Locate leukocytes (white blood cells).
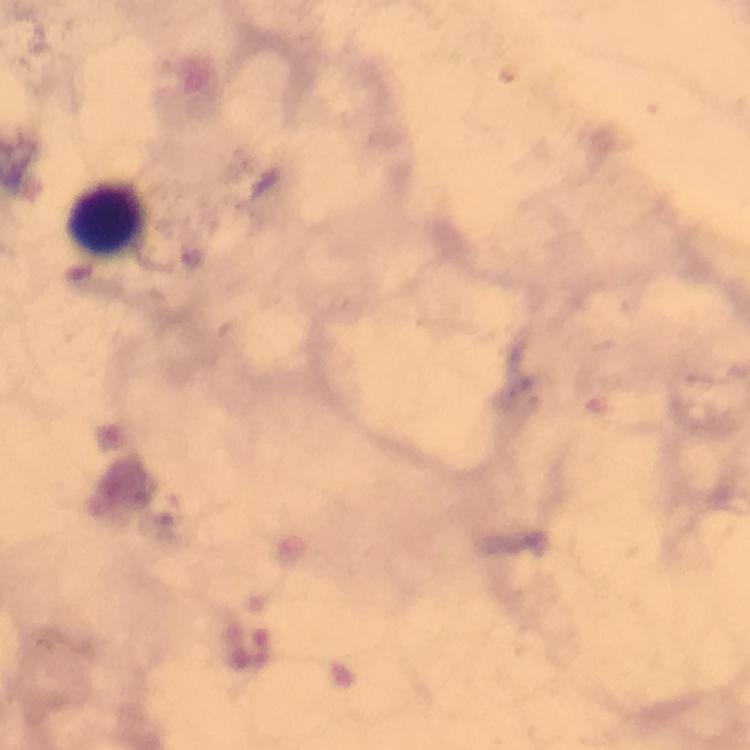

Approximate centers as {x, y} in pixels.
Leukocytes: {105, 221}.

immersion oil = used
image size = 750×750 pixels
cropped from = one field of view
context = from a malaria diagnostic workup
capture = smartphone photograph through a microscope
preparation = thick blood smear
malaria parasites = none detected
magnification = 100x
stain = Giemsa